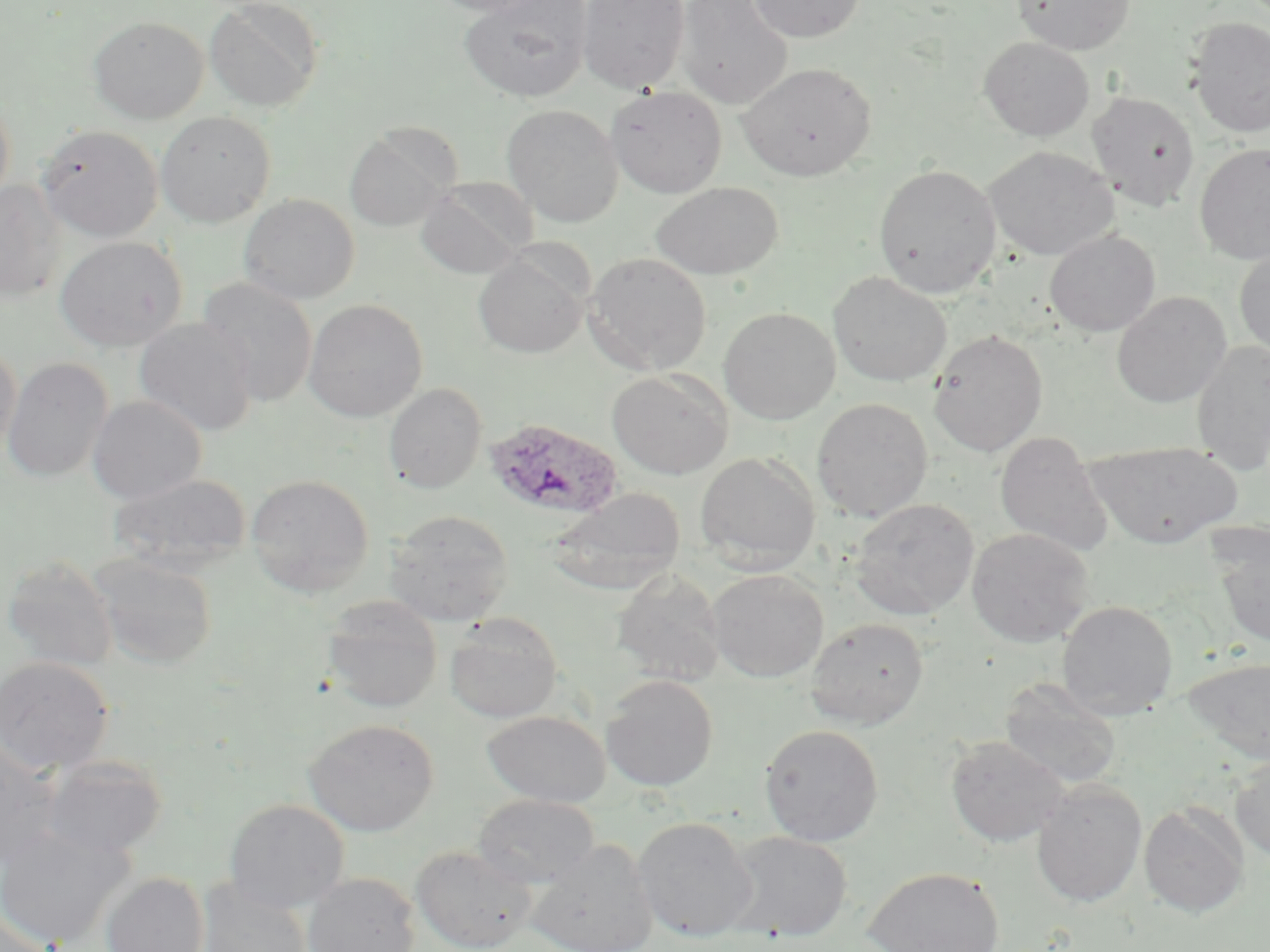
Summary:
  - Coordinate format: approximate bounding boxes as (x1,y1)-(x2,y2) corner pairs in pixels
  - Plasmodium ovale-infected red blood cell locations: (483,417)-(624,521)
  - Uninfected red blood cell locations: (204,0)-(324,111), (424,0)-(550,16), (458,0)-(593,102), (577,0)-(690,94), (675,0)-(794,109), (748,0)-(865,43), (1013,0)-(1135,55), (89,16)-(208,123), (1187,17)-(1270,138), (979,36)-(1095,141), (738,62)-(876,181), (606,85)-(727,198), (0,91)-(14,208), (1086,91)-(1201,212), (501,103)-(624,227), (155,110)-(276,228), (36,124)-(163,242), (343,127)-(457,232), (1193,144)-(1270,264), (984,146)-(1119,260), (873,163)-(1001,298), (415,178)-(537,279), (0,179)-(67,303), (650,181)-(784,280), (239,193)-(360,304), (1045,229)-(1161,336), (55,236)-(187,351), (1234,247)-(1270,359), (584,251)-(712,375), (473,252)-(590,358), (827,271)-(952,387), (197,277)-(318,407), (1111,291)-(1231,407), (303,298)-(428,422), (718,306)-(841,425), (134,318)-(258,437), (928,330)-(1048,456), (1191,341)-(1270,474), (0,345)-(21,457), (2,357)-(113,482), (607,369)-(733,479), (383,383)-(487,494), (86,395)-(207,504), (811,398)-(933,522), (994,432)-(1115,557), (1084,440)-(1242,548), (695,451)-(820,573), (107,472)-(252,574), (245,473)-(375,596), (546,488)-(686,595), (850,498)-(979,620), (384,509)-(513,626), (1205,524)-(1270,648), (966,528)-(1094,647), (88,552)-(218,671), (2,555)-(119,672), (708,569)-(828,682), (610,570)-(727,687), (321,597)-(443,714), (1056,600)-(1178,720), (444,614)-(564,722), (804,617)-(929,729), (0,656)-(114,774), (1181,657)-(1270,764), (600,674)-(719,791), (999,678)-(1122,789), (481,710)-(612,807), (304,718)-(439,836), (760,723)-(884,846), (946,735)-(1069,847), (0,740)-(64,869), (39,754)-(167,859), (1229,756)-(1270,861), (1032,780)-(1147,907), (472,793)-(600,889), (224,798)-(350,912), (1138,803)-(1249,917), (634,816)-(758,942), (0,823)-(134,948), (723,831)-(853,941), (525,838)-(658,952), (410,844)-(538,952), (864,866)-(1005,952), (101,872)-(210,952), (302,872)-(421,952), (196,879)-(313,952), (1,910)-(57,952)
  - Slide-level diagnosis: Plasmodium ovale
  - Modality: optical microscopy
  - Field of view: one of a larger specimen
  - Stain: May-Grünwald-Giemsa
  - Magnification: 1000x
  - Preparation: thin blood smear
  - Image size: 1270×952 pixels